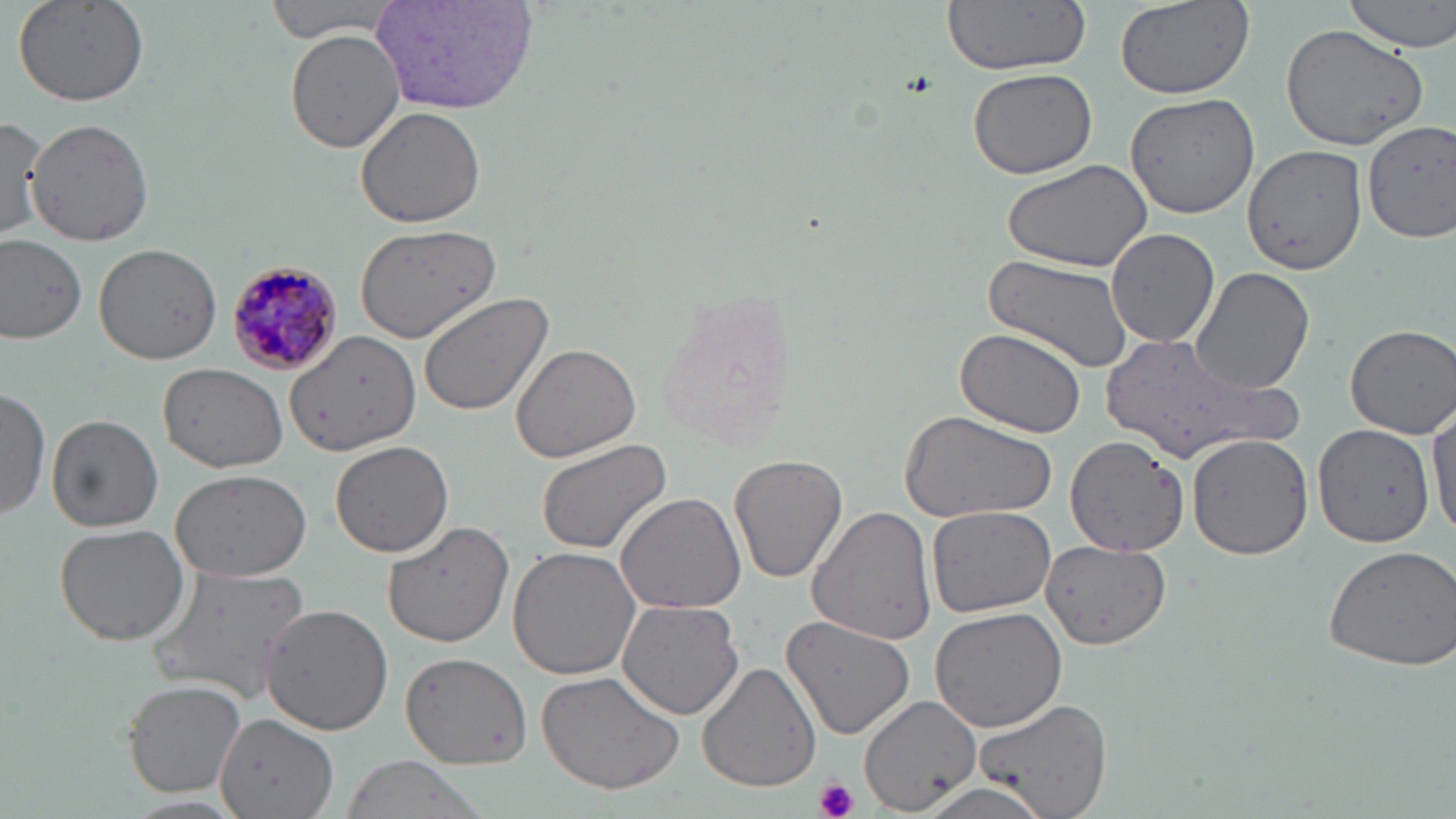
Approximate bounding boxes as (x1, y1, x2, y2) in pixels. Plasmodium malariae-infected red blood cell locations: (222, 259, 343, 379). Platelet locations: (814, 778, 858, 819). Uninfected red blood cell locations: (263, 0, 404, 42), (940, 0, 1092, 77), (1113, 0, 1255, 99), (1342, 0, 1456, 54), (11, 1, 149, 107), (369, 2, 542, 114), (1278, 23, 1428, 150), (284, 27, 405, 155), (965, 66, 1098, 180), (1125, 93, 1259, 218), (356, 105, 487, 227), (27, 117, 159, 247), (1, 118, 50, 237), (1362, 122, 1456, 240), (1240, 143, 1366, 271), (999, 157, 1154, 272), (356, 222, 501, 343), (1105, 227, 1219, 349), (0, 233, 88, 343), (93, 243, 223, 363), (978, 252, 1137, 374), (1191, 266, 1313, 397), (417, 292, 555, 416), (1344, 323, 1456, 439), (954, 326, 1090, 438), (285, 327, 421, 458), (1095, 330, 1293, 465), (509, 342, 641, 463), (158, 363, 289, 474), (0, 387, 50, 521), (1429, 401, 1455, 541), (899, 412, 1059, 523), (45, 415, 163, 532), (1312, 424, 1436, 548), (1186, 432, 1314, 558), (1068, 435, 1193, 556), (330, 437, 456, 557), (535, 439, 673, 556), (729, 453, 848, 583), (170, 467, 313, 580), (614, 491, 749, 614), (806, 502, 937, 647), (926, 505, 1058, 618), (382, 520, 515, 648), (55, 524, 191, 645), (1039, 541, 1171, 645), (1322, 544, 1456, 671), (507, 547, 645, 681), (144, 568, 310, 706), (616, 598, 745, 719), (256, 603, 394, 735), (928, 607, 1067, 732), (780, 611, 918, 741), (401, 651, 533, 771), (698, 661, 821, 792), (536, 669, 685, 793), (125, 679, 249, 799), (859, 691, 982, 813), (974, 696, 1112, 819), (217, 714, 340, 819), (344, 757, 478, 819), (912, 780, 1059, 819). Slide-level diagnosis: Plasmodium malariae. Thin blood film. May-Grünwald-Giemsa stain. Captured at 1000x magnification. One field of a larger specimen. Image is 1456×819 pixels. Optical microscopy.